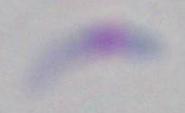

Photomicrograph. Toxoplasma gondii is seen. Captured at 1000x magnification.